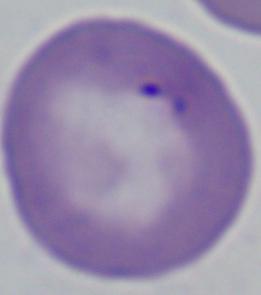

{
  "identification": "Babesia",
  "magnification": "1000x",
  "modality": "micrograph"
}